State which parasite is depicted.
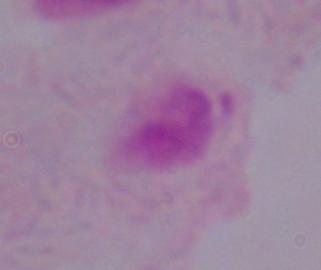
This is a trichomonad.

modality = photomicrograph
magnification = 1000x